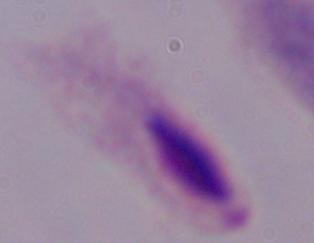
magnification: 1000x
modality: micrograph
identification: trichomonad